Locate every leukocyte (white blood cell).
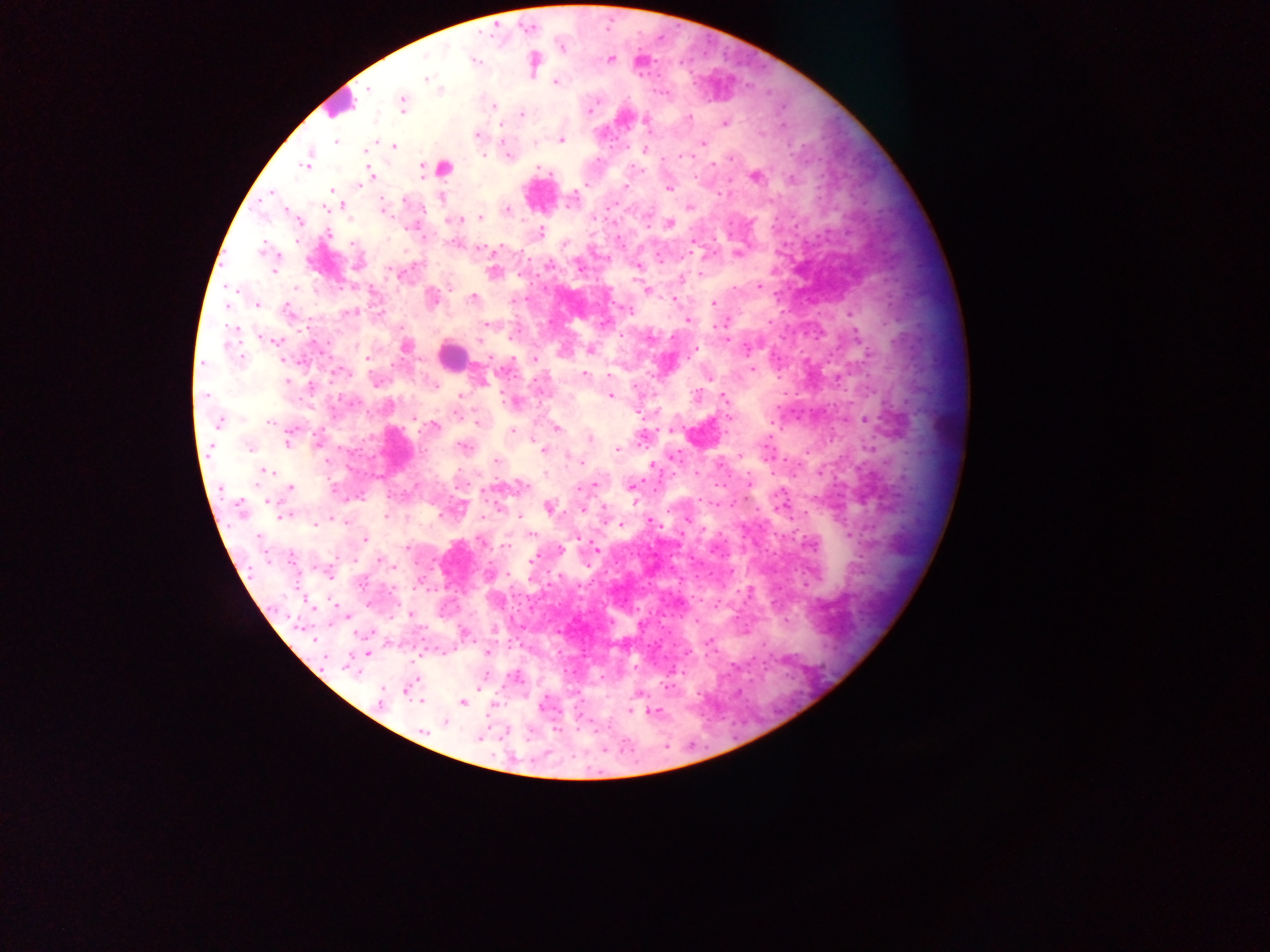
Approximate centers as [x, y] in pixels.
Leukocytes: [338, 104], [441, 167], [454, 356], [947, 426].

Plasmodium parasite locations: [561, 47], [474, 59], [610, 59], [534, 62], [425, 78], [555, 81], [367, 90], [440, 90], [402, 103], [495, 106], [521, 115], [688, 118], [645, 122], [724, 122], [476, 135], [560, 139], [336, 140], [703, 142], [393, 146], [645, 149], [366, 150], [683, 155], [508, 156], [308, 162], [370, 173], [755, 176], [790, 179], [624, 186], [668, 186], [330, 191], [271, 192], [440, 197], [404, 199], [341, 204], [327, 206], [687, 207], [384, 210], [507, 211], [480, 217], [458, 218], [669, 224], [540, 232], [328, 234], [353, 242], [693, 242], [481, 248], [264, 250], [738, 253], [358, 263], [636, 265], [274, 271], [493, 271], [701, 274], [681, 279], [759, 286], [231, 288], [647, 290], [430, 297], [472, 298], [671, 299], [712, 304], [227, 305], [257, 305], [628, 310], [286, 311], [353, 312], [687, 320], [487, 323], [235, 329], [725, 339], [275, 340], [405, 346], [590, 349], [368, 358], [282, 360], [534, 360], [751, 369], [337, 371], [585, 374], [608, 376], [708, 376], [375, 380], [482, 381], [433, 385], [204, 394], [460, 395], [610, 395], [722, 396], [514, 402], [458, 415], [415, 416], [728, 417], [863, 419], [271, 421], [219, 422], [477, 422], [433, 427], [557, 428], [671, 430], [512, 432], [590, 438], [288, 441], [250, 446], [463, 447], [617, 449], [543, 450], [740, 456], [495, 460], [581, 463], [653, 465], [263, 472], [591, 484], [522, 485], [630, 486], [289, 488], [268, 501], [548, 506], [239, 509], [583, 509], [282, 515], [520, 516], [687, 519], [650, 522], [315, 524], [621, 524], [848, 534], [530, 535], [576, 536], [365, 538], [595, 548], [559, 550], [291, 555], [530, 560], [344, 614], [410, 614], [464, 633], [487, 653], [367, 654], [350, 668], [407, 689], [638, 693], [422, 700], [462, 701], [380, 702], [543, 706], [630, 709], [652, 712], [444, 721], [423, 730], [479, 738]. Image is 1270×952 pixels. Sample from Ghana. Thick blood film. One field of view. Photographed through a microscope with a mobile-phone camera.